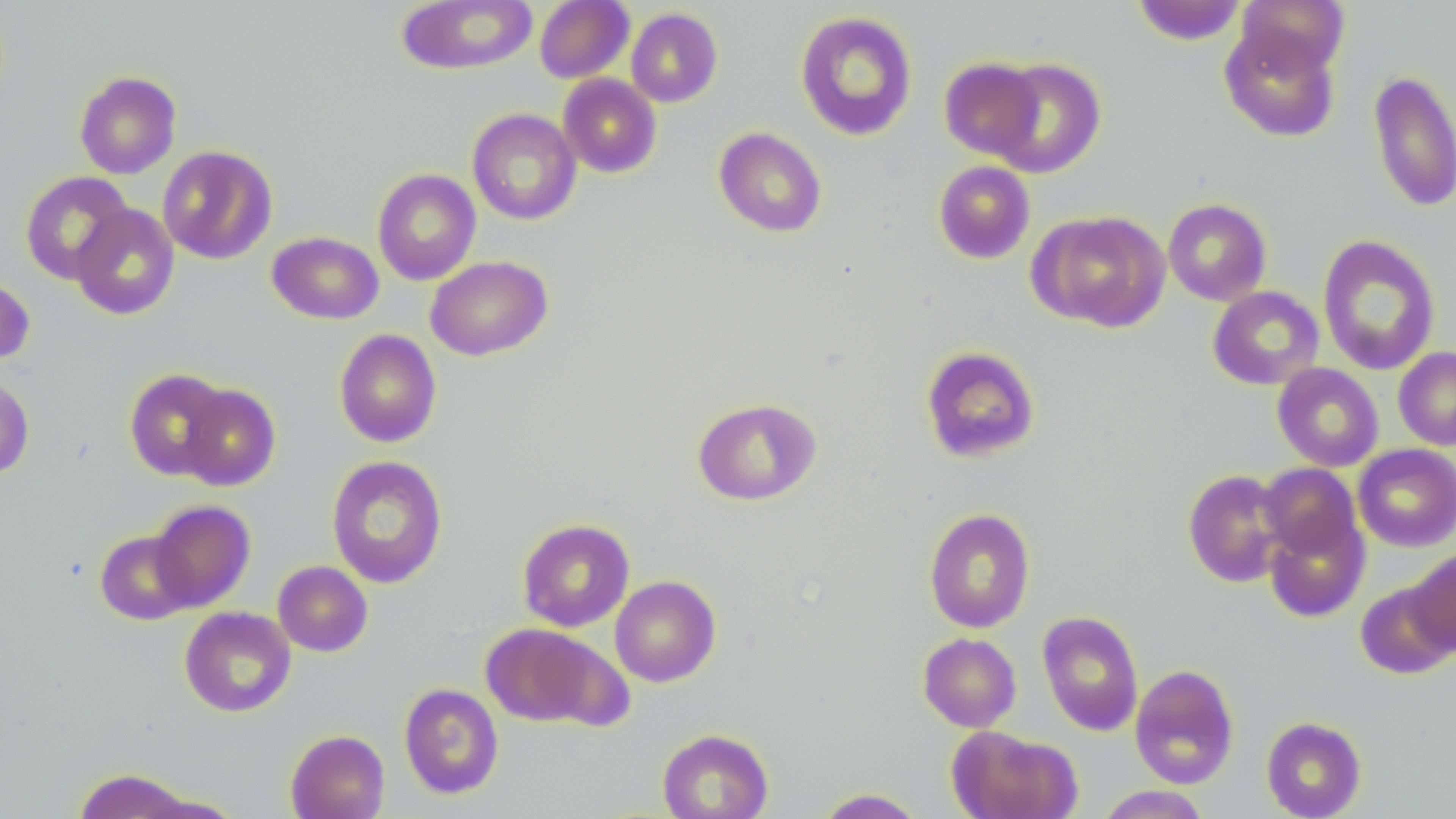

{
  "slide_level_diagnosis": "negative for blood parasites",
  "image_size": "1456×819 pixels",
  "stain": "May-Grünwald-Giemsa",
  "uninfected_red_blood_cell_locations": "approximate bounding boxes as (x1, y1, x2, y2) in pixels: (397, 0, 538, 75), (1131, 0, 1248, 45), (1235, 0, 1350, 79), (534, 1, 634, 83), (626, 7, 722, 107), (794, 10, 918, 141), (1219, 22, 1341, 142), (939, 57, 1044, 161), (989, 57, 1107, 178), (1368, 69, 1455, 213), (74, 70, 181, 179), (558, 74, 662, 178), (467, 108, 582, 225), (714, 127, 827, 237), (157, 145, 278, 264), (933, 160, 1035, 264), (372, 168, 482, 285), (19, 170, 134, 285), (1163, 198, 1272, 306), (71, 203, 180, 320), (1028, 209, 1170, 333), (267, 231, 384, 324), (1317, 234, 1441, 376), (426, 255, 552, 361), (0, 274, 35, 366), (1207, 286, 1324, 390), (334, 328, 442, 448), (921, 345, 1040, 463), (1393, 347, 1456, 451), (1272, 363, 1384, 471), (124, 368, 231, 480), (0, 373, 35, 480), (178, 384, 281, 491), (692, 397, 822, 506), (1353, 444, 1456, 552), (326, 455, 448, 589), (1257, 463, 1361, 562), (1182, 469, 1290, 587), (148, 500, 255, 611), (923, 507, 1036, 633), (1263, 511, 1370, 623), (517, 518, 635, 632), (94, 529, 197, 625), (1409, 547, 1456, 656), (273, 560, 373, 656), (610, 575, 721, 687), (1355, 580, 1456, 680), (179, 606, 296, 717), (1037, 610, 1144, 736), (480, 622, 626, 730), (918, 632, 1021, 732), (1130, 664, 1239, 789), (399, 683, 503, 800), (1261, 716, 1367, 818), (946, 725, 1081, 819), (657, 728, 774, 819), (285, 729, 390, 819), (72, 768, 196, 819), (1095, 785, 1212, 818), (814, 788, 928, 818)",
  "modality": "light microscopy",
  "preparation": "thin blood smear",
  "magnification": "1000x",
  "field_of_view": "single"
}